Name the parasite shown.
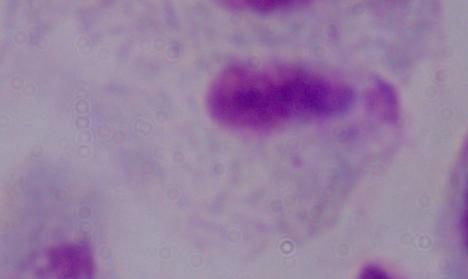

This is a trichomonad.

magnification = 1000x
modality = photomicrograph